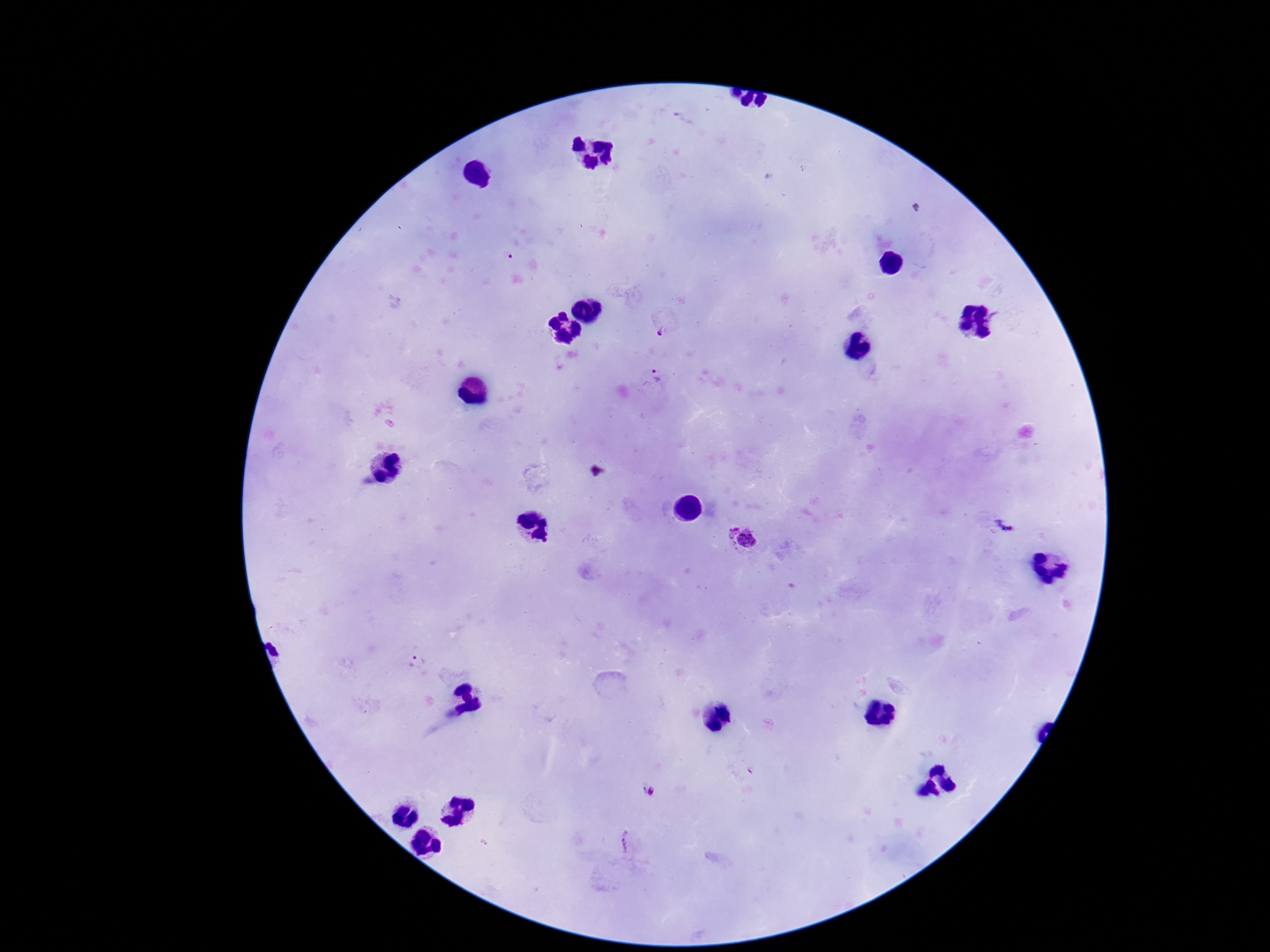
field_of_view: one from this slide
preparation: thick blood smear
patient_malaria_status: positive
capture: smartphone camera through the microscope eyepiece
plasmodium_parasite_locations: 'approximate centers as [x, y] in pixels: [657, 376], [741, 538], [649, 791], [626, 842]'
magnification: 100x
image_size: 1270×952 pixels
stain: Giemsa